Describe the morphology of the erythrocytes.
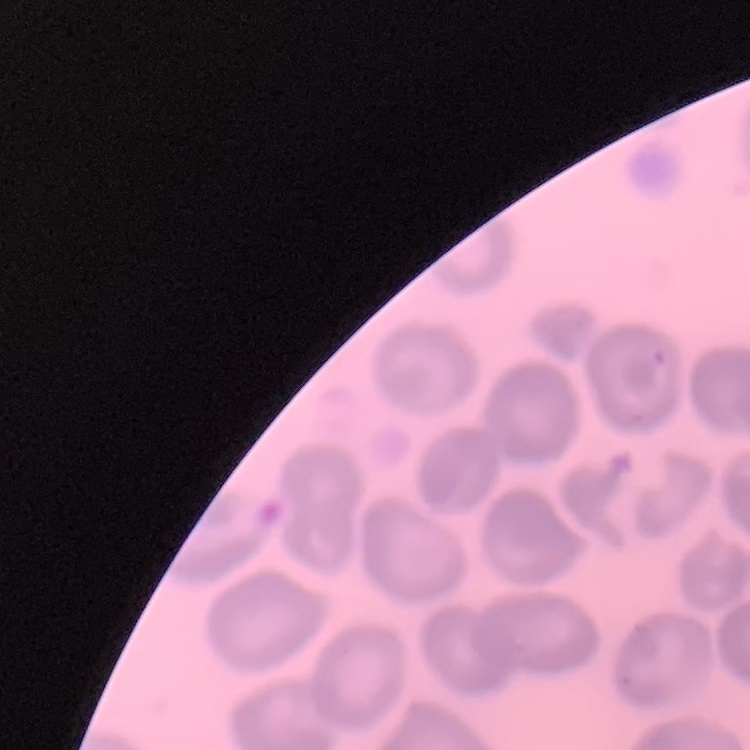
No rouleaux formation.

stain = Field's or Giemsa
image type = square crop of a larger photomicrograph
preparation = thin blood film